Assess this cell for malaria.
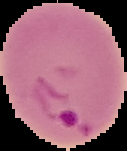
It is parasitized.

Summary:
  - Image type: segmented cell region on a black background
  - Preparation: thin blood film
  - Image size: 127×151 pixels